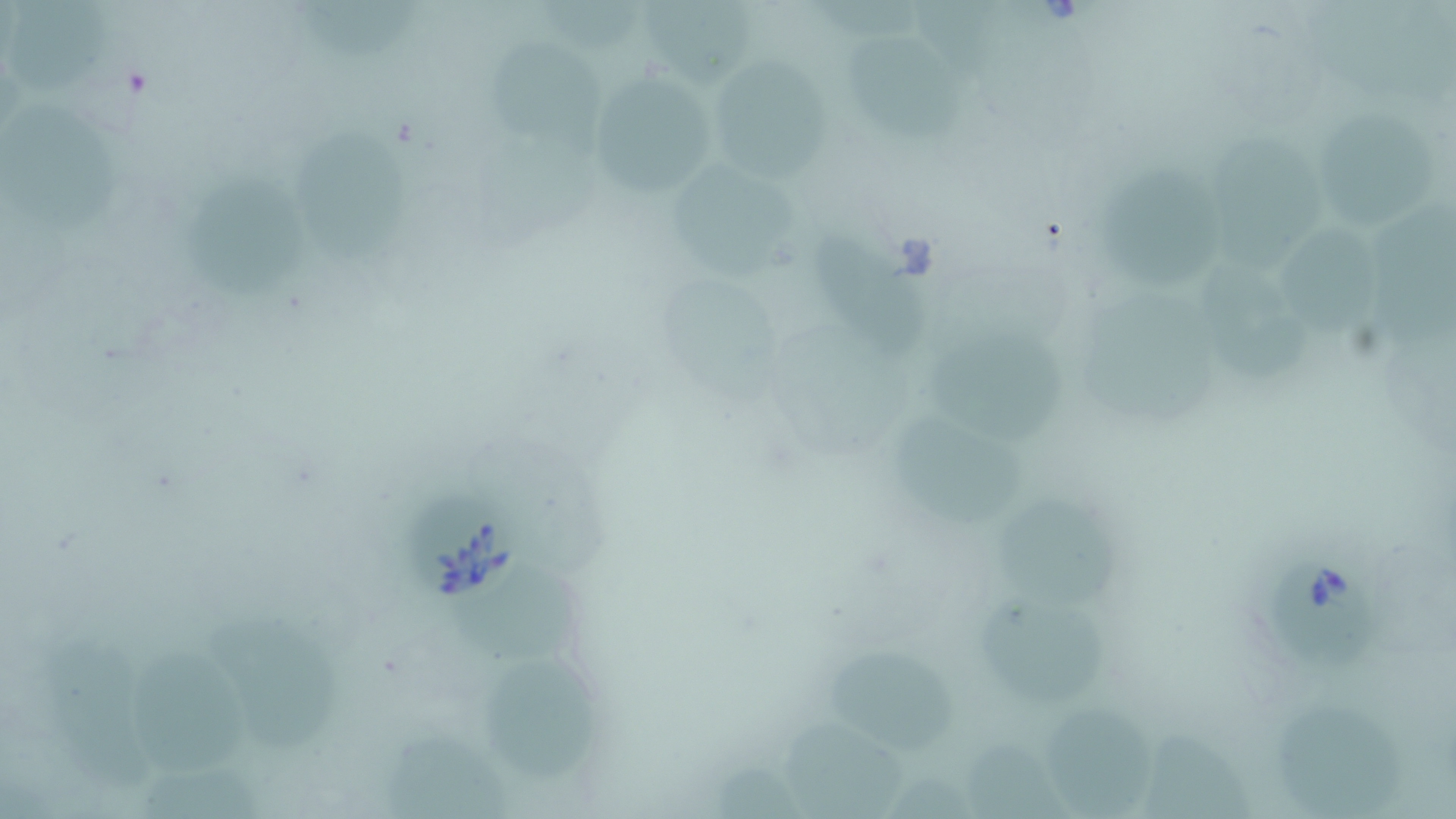

Approximate bounding boxes as (x1, y1, x2, y2) in pixels. Babesia divergens-infected red blood cell locations: (397, 474, 524, 605), (1267, 550, 1382, 670). Uninfected red blood cell locations: (6, 1, 117, 94), (291, 1, 418, 62), (631, 6, 757, 86), (841, 34, 967, 142), (482, 35, 600, 139), (709, 57, 832, 182), (585, 67, 719, 200), (1313, 99, 1441, 231), (1, 101, 121, 233), (291, 124, 417, 267), (1209, 134, 1322, 265), (1098, 161, 1229, 290), (666, 162, 802, 270), (183, 167, 304, 302), (1374, 195, 1456, 348), (1282, 221, 1385, 341), (817, 234, 930, 361), (1196, 257, 1312, 386), (661, 266, 783, 409), (1083, 287, 1223, 422), (932, 325, 1063, 445), (888, 415, 1022, 530), (1000, 488, 1123, 609), (445, 572, 584, 666), (976, 595, 1110, 709), (207, 609, 342, 753), (43, 629, 157, 790), (127, 640, 256, 775), (829, 651, 957, 754), (483, 652, 593, 776), (1275, 694, 1408, 815), (1044, 697, 1154, 817), (776, 716, 908, 819), (1138, 721, 1259, 817), (381, 728, 516, 818), (966, 736, 1064, 818), (138, 752, 266, 819). Slide-level diagnosis: Babesia divergens. Light microscopy. May-Grünwald-Giemsa stain. One field of a larger specimen. Thin blood film. Image is 1456×819 pixels. 1000x magnification.